Locate every blood parasite and identify its species.
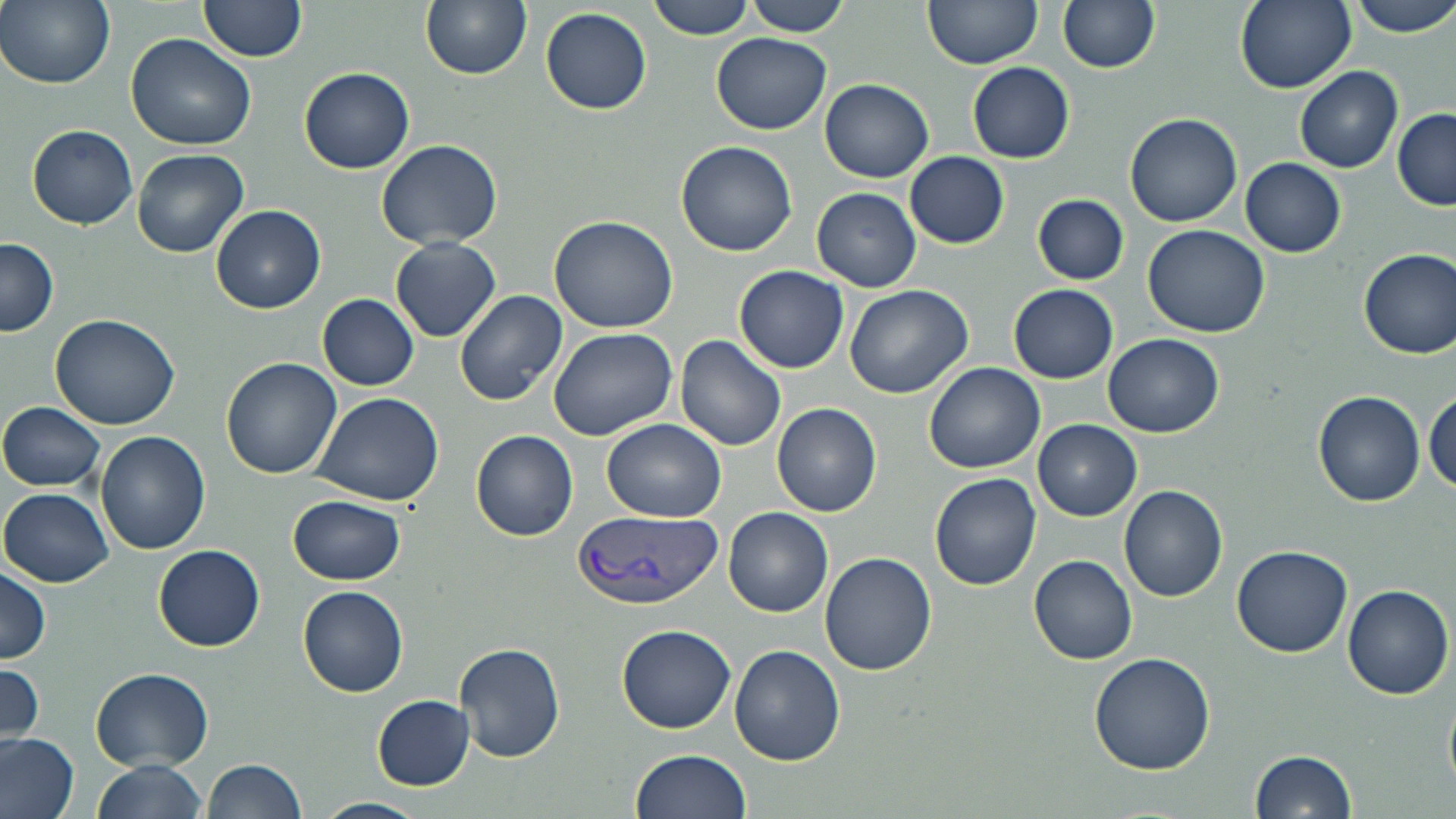
Approximate bounding boxes as named x1/y1/x2/y2 corners in pixels.
Plasmodium vivax-infected red blood cells: (x1=575, y1=508, x2=721, y2=610).
No Plasmodium falciparum, Plasmodium ovale, Plasmodium malariae, Babesia divergens, or Trypanosoma brucei observed.

Summary:
  - Uninfected red blood cell locations: (x1=1, y1=0, x2=115, y2=90), (x1=197, y1=0, x2=308, y2=62), (x1=420, y1=0, x2=531, y2=79), (x1=648, y1=0, x2=758, y2=41), (x1=921, y1=0, x2=1042, y2=70), (x1=1058, y1=0, x2=1160, y2=74), (x1=1234, y1=0, x2=1356, y2=93), (x1=1347, y1=0, x2=1456, y2=37), (x1=740, y1=1, x2=851, y2=36), (x1=539, y1=6, x2=652, y2=114), (x1=125, y1=31, x2=258, y2=151), (x1=710, y1=34, x2=834, y2=135), (x1=967, y1=61, x2=1076, y2=164), (x1=1295, y1=65, x2=1402, y2=173), (x1=300, y1=66, x2=415, y2=173), (x1=820, y1=79, x2=934, y2=183), (x1=1391, y1=108, x2=1456, y2=212), (x1=1125, y1=111, x2=1242, y2=227), (x1=27, y1=125, x2=138, y2=229), (x1=375, y1=138, x2=504, y2=250), (x1=675, y1=141, x2=798, y2=257), (x1=131, y1=147, x2=249, y2=257), (x1=904, y1=151, x2=1009, y2=247), (x1=1240, y1=158, x2=1346, y2=257), (x1=813, y1=186, x2=921, y2=292), (x1=1034, y1=194, x2=1128, y2=284), (x1=210, y1=204, x2=326, y2=314), (x1=549, y1=214, x2=679, y2=333), (x1=1142, y1=223, x2=1272, y2=337), (x1=391, y1=237, x2=501, y2=341), (x1=1, y1=238, x2=60, y2=338), (x1=1358, y1=248, x2=1456, y2=357), (x1=735, y1=265, x2=849, y2=373), (x1=844, y1=283, x2=973, y2=399), (x1=1008, y1=283, x2=1119, y2=383), (x1=455, y1=290, x2=567, y2=406), (x1=317, y1=294, x2=420, y2=390), (x1=50, y1=311, x2=183, y2=430), (x1=546, y1=326, x2=677, y2=441), (x1=1102, y1=333, x2=1224, y2=439), (x1=676, y1=335, x2=788, y2=451), (x1=220, y1=358, x2=341, y2=478), (x1=924, y1=362, x2=1044, y2=475), (x1=309, y1=390, x2=445, y2=507), (x1=1426, y1=390, x2=1455, y2=497), (x1=1314, y1=392, x2=1426, y2=506), (x1=0, y1=402, x2=107, y2=491), (x1=772, y1=402, x2=881, y2=517), (x1=602, y1=418, x2=725, y2=523), (x1=1034, y1=420, x2=1141, y2=521), (x1=471, y1=430, x2=578, y2=541), (x1=96, y1=432, x2=209, y2=555), (x1=929, y1=473, x2=1042, y2=590), (x1=1118, y1=484, x2=1228, y2=602), (x1=1, y1=488, x2=113, y2=587), (x1=288, y1=495, x2=405, y2=585), (x1=723, y1=507, x2=833, y2=617), (x1=1232, y1=543, x2=1353, y2=657), (x1=154, y1=544, x2=265, y2=651), (x1=819, y1=552, x2=938, y2=678), (x1=1030, y1=554, x2=1137, y2=665), (x1=0, y1=566, x2=51, y2=664), (x1=1341, y1=584, x2=1453, y2=700), (x1=298, y1=586, x2=408, y2=694), (x1=618, y1=622, x2=736, y2=733), (x1=454, y1=640, x2=567, y2=763), (x1=729, y1=646, x2=845, y2=766), (x1=1090, y1=651, x2=1214, y2=774), (x1=0, y1=662, x2=46, y2=749), (x1=90, y1=668, x2=215, y2=772), (x1=373, y1=695, x2=475, y2=788), (x1=0, y1=733, x2=80, y2=819), (x1=1249, y1=748, x2=1358, y2=819), (x1=627, y1=750, x2=752, y2=819), (x1=92, y1=758, x2=212, y2=819), (x1=203, y1=759, x2=308, y2=818), (x1=312, y1=797, x2=427, y2=819)
  - Slide-level diagnosis: Plasmodium vivax
  - Stain: May-Grünwald-Giemsa
  - Modality: optical microscopy
  - Magnification: 1000x
  - Preparation: thin blood film
  - Image size: 1456×819 pixels
  - Field of view: single